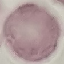

Malaria status: uninfected. Acquired by smartphone through the microscope eyepiece. Thin smear of blood. Giemsa stain. Automatically extracted cell patch, resized to 64 × 64 pixels.